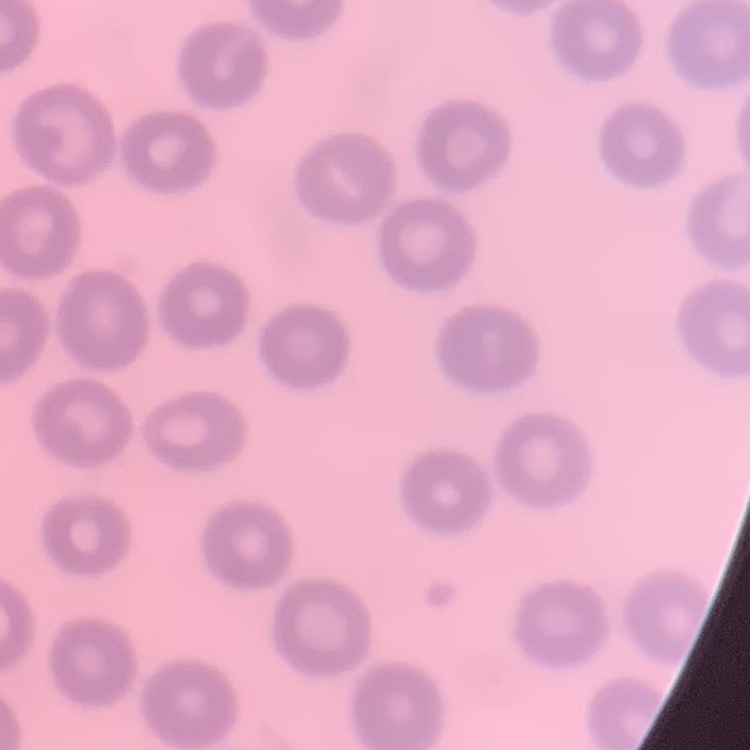
The red blood cells exhibit no rouleaux formation. One tile cut from a larger photomicrograph. Stained with either Field's or Giemsa. Thin blood film.